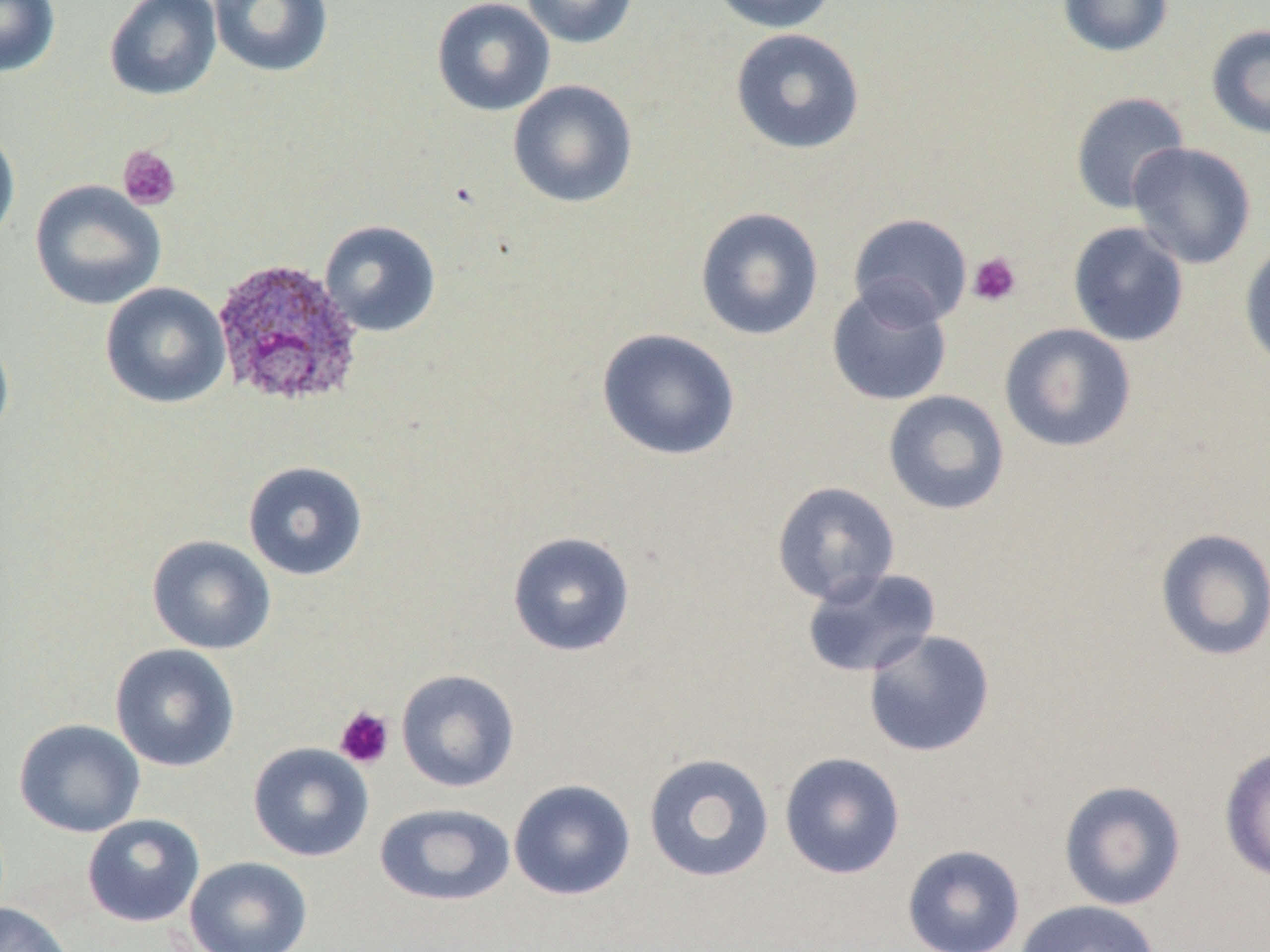
Summary:
  - Coordinate format: approximate bounding boxes as [x1, y1, x2, y2] in pixels
  - Platelet locations: [117, 144, 181, 211], [967, 252, 1022, 307], [334, 705, 395, 769]
  - Uninfected red blood cell locations: [0, 0, 60, 78], [104, 0, 223, 101], [209, 0, 333, 78], [431, 0, 555, 116], [521, 0, 638, 49], [707, 0, 837, 33], [1058, 0, 1174, 57], [1206, 24, 1270, 140], [730, 28, 865, 155], [508, 80, 638, 208], [1070, 91, 1190, 214], [0, 124, 20, 249], [1127, 141, 1257, 270], [30, 180, 166, 310], [695, 206, 824, 341], [848, 213, 973, 328], [319, 220, 441, 337], [1068, 222, 1190, 347], [1239, 242, 1270, 370], [100, 282, 231, 409], [827, 282, 953, 407], [999, 323, 1137, 452], [0, 328, 14, 448], [596, 328, 742, 461], [883, 390, 1010, 516], [242, 460, 368, 581], [771, 481, 900, 606], [1153, 527, 1270, 663], [507, 531, 636, 657], [146, 535, 276, 655], [800, 566, 941, 679], [863, 629, 996, 758], [109, 643, 241, 772], [395, 669, 520, 792], [13, 718, 145, 838], [248, 742, 373, 861], [1219, 744, 1270, 883], [778, 751, 906, 880], [642, 752, 775, 883], [508, 779, 636, 900], [1058, 780, 1187, 911], [374, 802, 516, 906], [82, 813, 206, 928], [902, 844, 1025, 952], [184, 856, 313, 952], [1015, 899, 1162, 952], [0, 902, 74, 952]
  - Plasmodium ovale-infected red blood cell locations: [210, 257, 365, 410]
  - Slide-level diagnosis: Plasmodium ovale
  - Field of view: one of a larger specimen
  - Stain: May-Grünwald-Giemsa
  - Image size: 1270×952 pixels
  - Magnification: 1000x
  - Modality: optical microscopy
  - Preparation: thin blood smear